Identify the parasite.
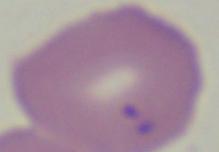
This is Babesia.

modality = micrograph
magnification = 1000x